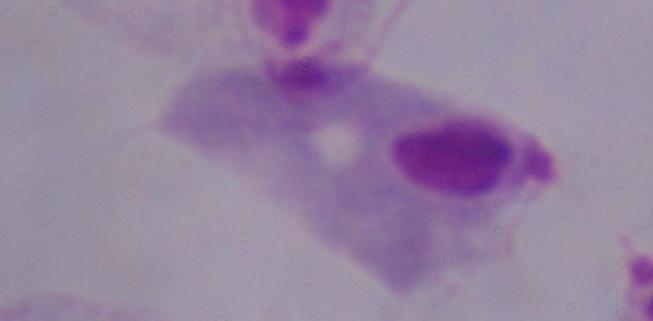
modality = photomicrograph
identification = trichomonad
magnification = 1000x